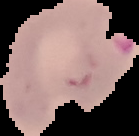 The area outside the segmented cell region is set to black. Result: Plasmodium parasites detected. From a thin blood smear. Image is 139×136 pixels.